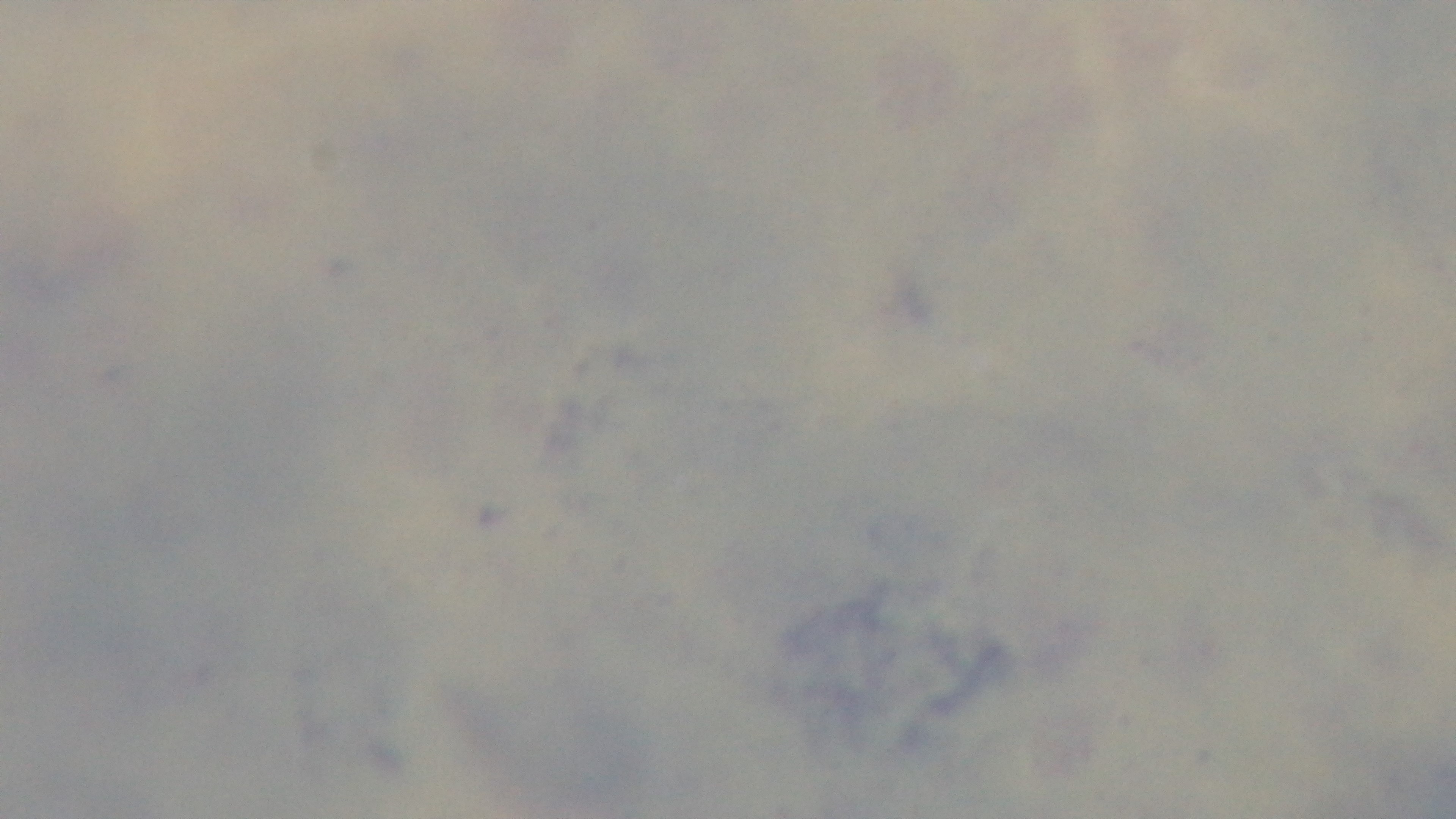 Preparation: thick. Malaria status: negative. Giemsa-stained. Photomicrograph. 100x oil-immersion objective. Single field of view. Mounted 4K digital camera.